Give the extent of all uninfected red blood cells.
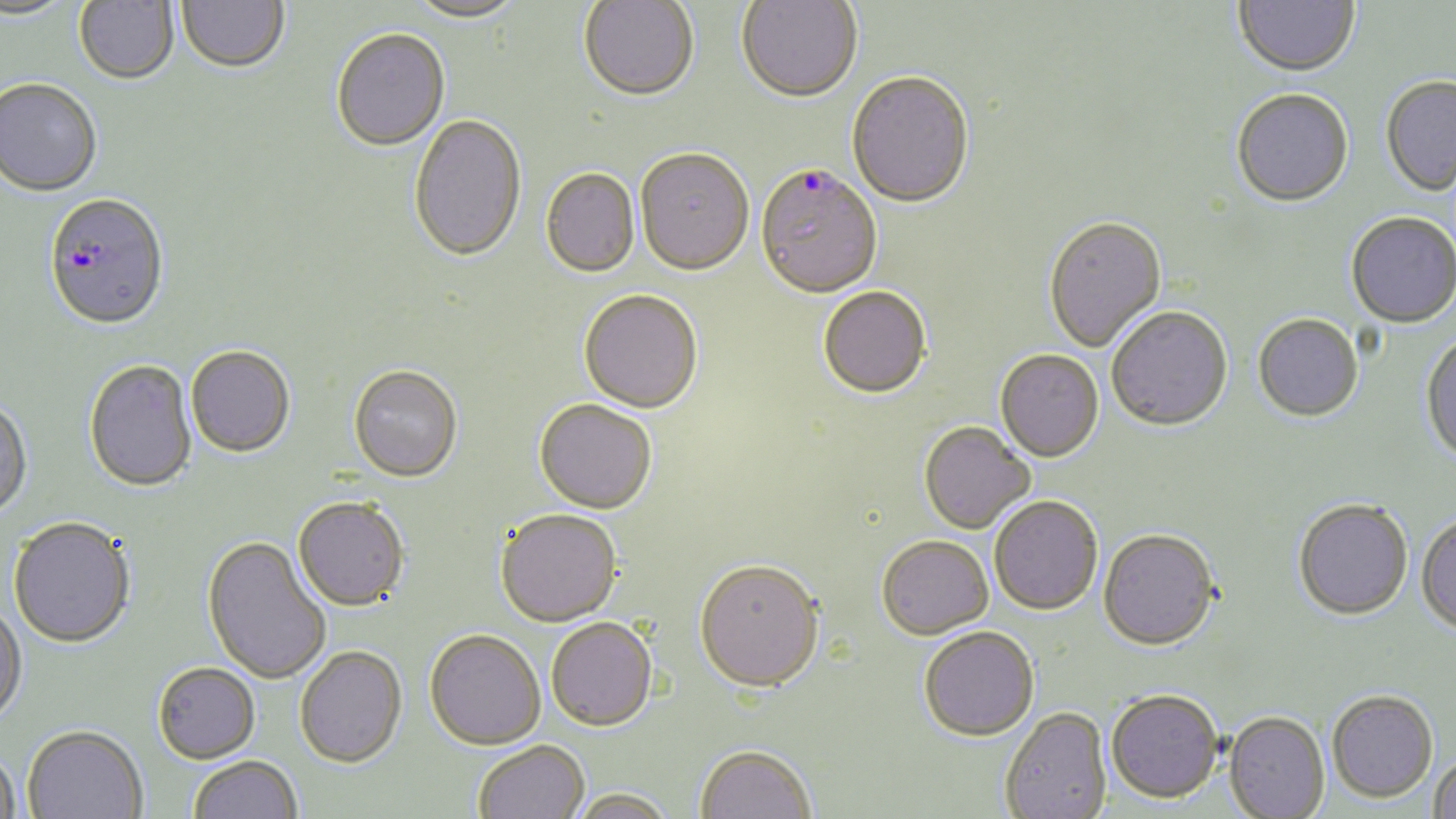

Approximate bounding boxes as [x1, y1, x2, y2] in pixels.
Uninfected red blood cells: [0, 0, 77, 22], [75, 0, 179, 84], [404, 0, 528, 25], [579, 0, 699, 103], [1234, 0, 1359, 79], [177, 1, 290, 73], [736, 1, 862, 105], [331, 29, 450, 153], [847, 74, 975, 210], [0, 78, 102, 197], [1381, 78, 1456, 198], [1231, 91, 1354, 210], [408, 116, 527, 265], [635, 150, 754, 277], [541, 169, 640, 278], [1346, 214, 1456, 330], [1043, 218, 1167, 354], [818, 288, 932, 400], [579, 290, 703, 414], [1107, 309, 1233, 434], [1253, 316, 1364, 424], [1421, 333, 1456, 466], [186, 346, 295, 458], [995, 351, 1104, 464], [83, 359, 197, 493], [347, 365, 463, 482], [0, 397, 32, 521], [534, 399, 657, 515], [918, 422, 1035, 535], [293, 496, 409, 611], [989, 497, 1103, 617], [1292, 501, 1413, 623], [495, 510, 622, 627], [1415, 515, 1456, 637], [7, 518, 136, 649], [1098, 530, 1220, 654], [202, 535, 331, 684], [877, 537, 993, 641], [694, 562, 825, 696], [0, 602, 27, 724], [546, 618, 658, 732], [919, 628, 1040, 743], [425, 630, 545, 751], [295, 646, 407, 769], [153, 662, 260, 763], [1105, 690, 1224, 805], [1327, 691, 1439, 804], [1000, 708, 1111, 819], [1224, 713, 1330, 818], [22, 726, 148, 818], [474, 741, 590, 819], [695, 747, 816, 819], [0, 749, 21, 818], [1429, 754, 1456, 819], [189, 756, 302, 819], [569, 789, 677, 819].

Summary:
  - Plasmodium falciparum-infected red blood cell locations: [755, 166, 882, 300], [43, 193, 170, 331]
  - Slide-level diagnosis: Plasmodium falciparum
  - Magnification: 1000x
  - Preparation: thin blood smear
  - Modality: light microscopy
  - Field of view: one of a larger specimen
  - Stain: May-Grünwald-Giemsa
  - Image size: 1456×819 pixels